Locate every blood parasite and identify its species.
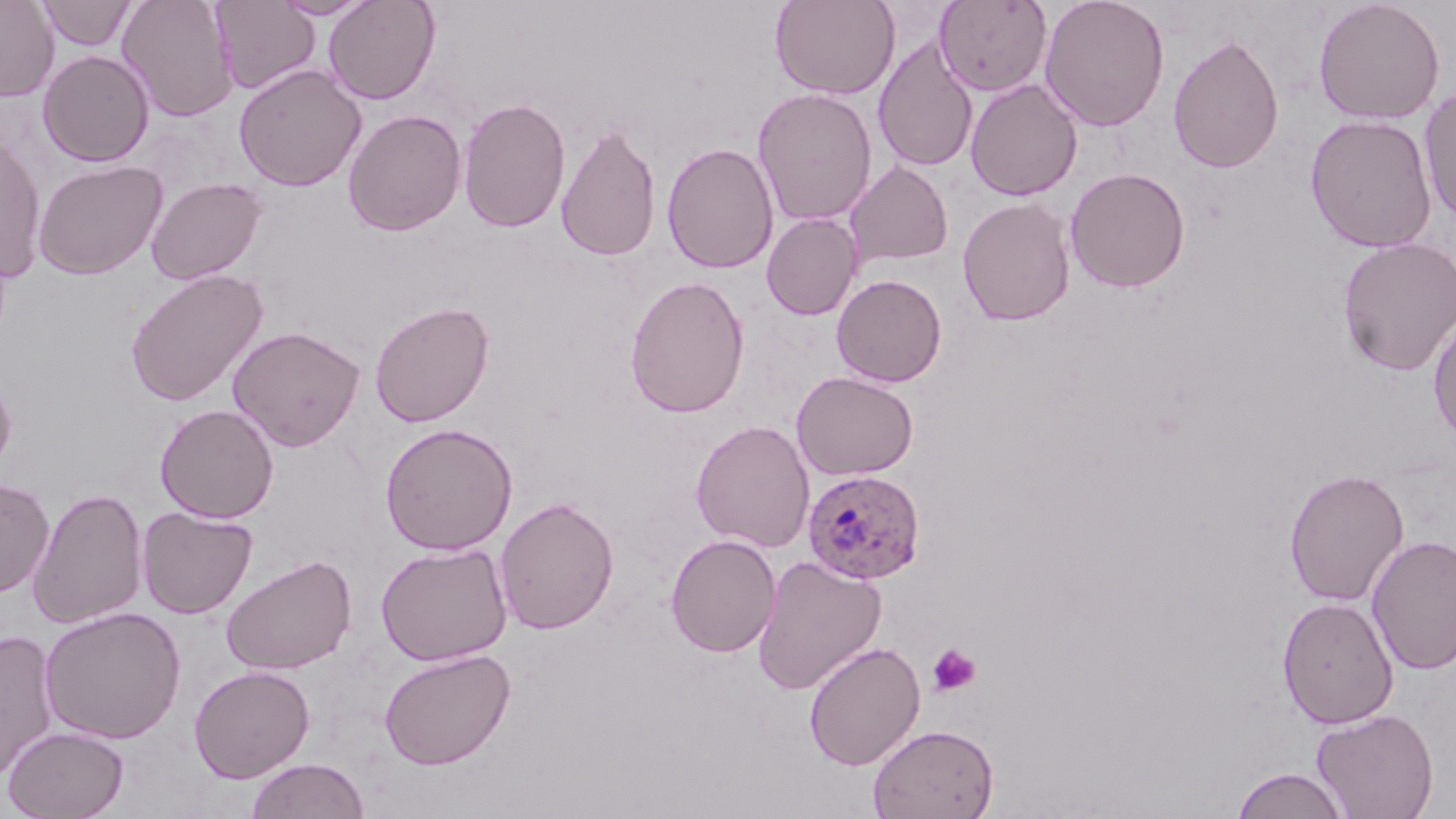
Approximate bounding boxes as named x1/y1/x2/y2 corners in pixels.
Plasmodium ovale-infected red blood cells: (x1=802, y1=468, x2=927, y2=584).
No Plasmodium falciparum, Plasmodium malariae, Plasmodium vivax, Babesia divergens, or Trypanosoma brucei observed.

Uninfected red blood cell locations: (x1=0, y1=0, x2=59, y2=101), (x1=116, y1=0, x2=239, y2=122), (x1=272, y1=0, x2=376, y2=19), (x1=323, y1=0, x2=441, y2=105), (x1=770, y1=0, x2=901, y2=99), (x1=934, y1=0, x2=1052, y2=96), (x1=1038, y1=0, x2=1170, y2=132), (x1=1313, y1=0, x2=1445, y2=124), (x1=36, y1=1, x2=137, y2=51), (x1=211, y1=1, x2=320, y2=95), (x1=1168, y1=32, x2=1284, y2=175), (x1=873, y1=36, x2=979, y2=173), (x1=38, y1=50, x2=154, y2=167), (x1=233, y1=63, x2=367, y2=192), (x1=965, y1=78, x2=1083, y2=202), (x1=1418, y1=86, x2=1456, y2=223), (x1=752, y1=88, x2=878, y2=226), (x1=457, y1=97, x2=572, y2=233), (x1=343, y1=109, x2=466, y2=236), (x1=1304, y1=114, x2=1438, y2=253), (x1=556, y1=122, x2=662, y2=262), (x1=0, y1=132, x2=46, y2=282), (x1=662, y1=142, x2=779, y2=274), (x1=33, y1=159, x2=167, y2=280), (x1=845, y1=161, x2=953, y2=267), (x1=1064, y1=167, x2=1191, y2=293), (x1=146, y1=176, x2=266, y2=284), (x1=957, y1=197, x2=1077, y2=327), (x1=762, y1=213, x2=863, y2=320), (x1=1336, y1=236, x2=1456, y2=376), (x1=124, y1=268, x2=269, y2=407), (x1=831, y1=273, x2=947, y2=387), (x1=624, y1=275, x2=750, y2=418), (x1=369, y1=300, x2=495, y2=428), (x1=1427, y1=309, x2=1456, y2=447), (x1=228, y1=325, x2=366, y2=452), (x1=0, y1=367, x2=17, y2=477), (x1=791, y1=371, x2=919, y2=481), (x1=155, y1=404, x2=279, y2=523), (x1=691, y1=419, x2=815, y2=552), (x1=380, y1=422, x2=518, y2=556), (x1=1283, y1=467, x2=1409, y2=607), (x1=0, y1=478, x2=55, y2=597), (x1=28, y1=487, x2=149, y2=629), (x1=495, y1=496, x2=619, y2=635), (x1=137, y1=505, x2=258, y2=619), (x1=665, y1=533, x2=781, y2=657), (x1=1367, y1=534, x2=1456, y2=675), (x1=375, y1=543, x2=513, y2=666), (x1=220, y1=553, x2=358, y2=674), (x1=751, y1=555, x2=887, y2=695), (x1=1277, y1=596, x2=1399, y2=729), (x1=39, y1=606, x2=187, y2=745), (x1=0, y1=628, x2=60, y2=782), (x1=804, y1=641, x2=926, y2=770), (x1=378, y1=648, x2=517, y2=771), (x1=188, y1=665, x2=316, y2=782), (x1=1311, y1=707, x2=1439, y2=819), (x1=867, y1=723, x2=999, y2=819), (x1=2, y1=725, x2=129, y2=818), (x1=244, y1=758, x2=371, y2=819), (x1=1230, y1=767, x2=1351, y2=818). Platelet locations: (x1=928, y1=643, x2=981, y2=696). Slide-level diagnosis: Plasmodium ovale. Image is 1456×819 pixels. May-Grünwald-Giemsa-stained preparation. Thin blood film. Captured at 1000x magnification. Light microscopy. One field of a larger specimen.